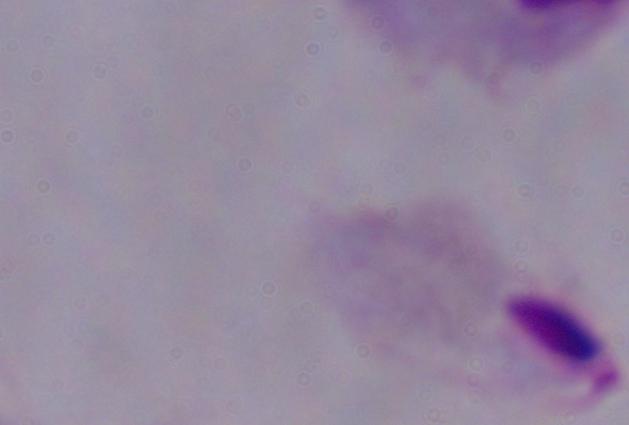

identification = trichomonad
modality = micrograph
magnification = 1000x